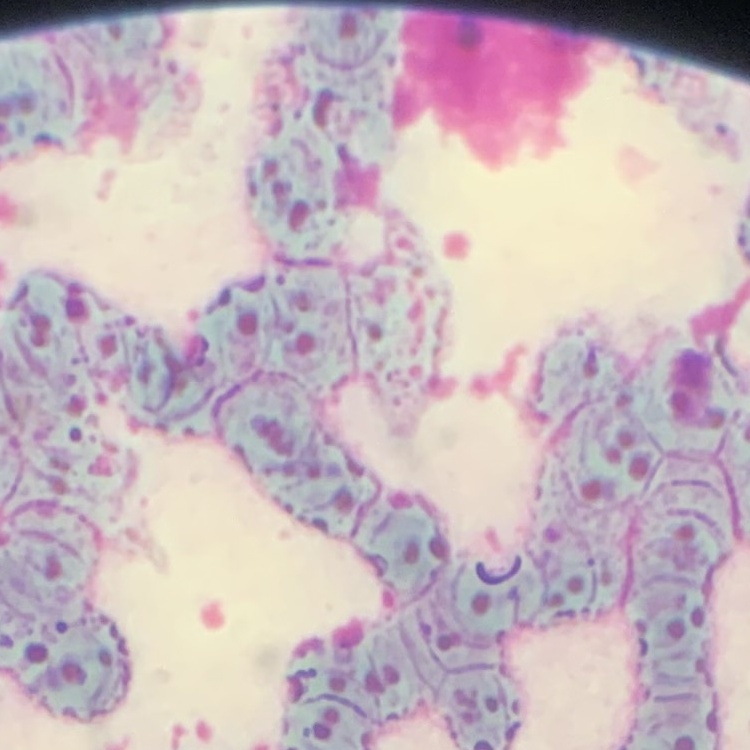
Summary:
  - Red blood cell morphology: rouleaux formation
  - Stain: Field's or Giemsa
  - Image type: square crop of a larger photomicrograph
  - Preparation: thin blood film